State which parasite is depicted.
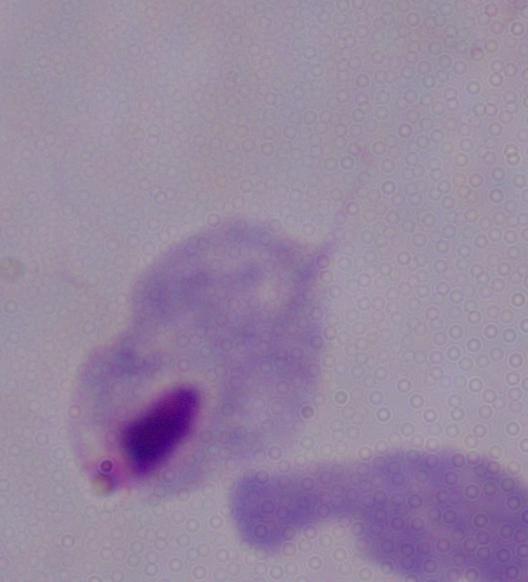
A trichomonad.

modality = micrograph
magnification = 1000x